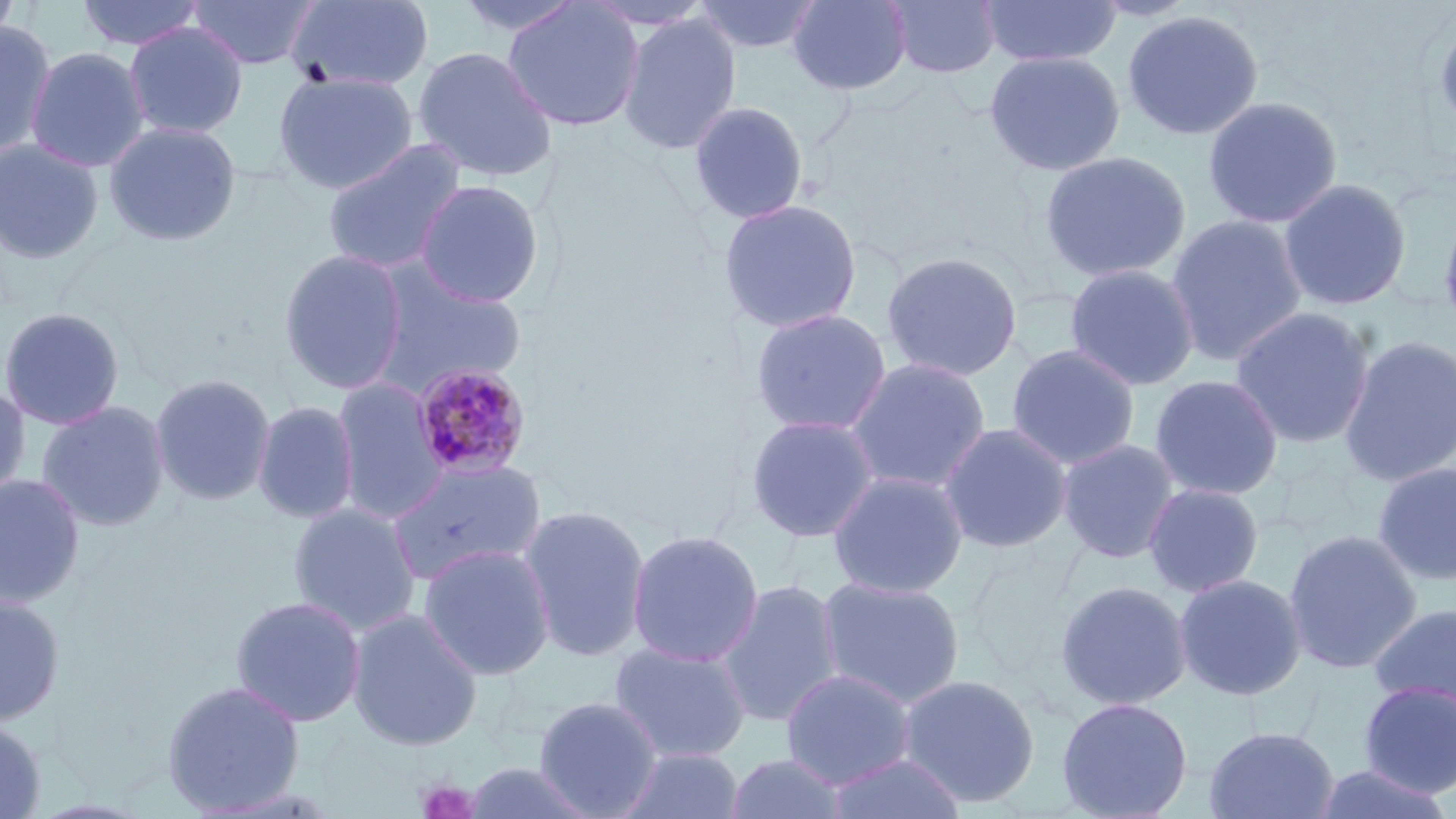
slide-level diagnosis = Plasmodium malariae
modality = light microscopy
magnification = 1000x
stain = May-Grünwald-Giemsa
uninfected red blood cell locations = approximate bounding boxes as (x1,y1)-(x2,y2) corner pairs in pixels: (0,0)-(21,52), (74,0)-(207,52), (185,0)-(321,70), (285,0)-(436,93), (455,0)-(585,39), (502,0)-(645,132), (692,0)-(824,55), (787,0)-(912,95), (886,0)-(1002,79), (979,0)-(1122,67), (1122,10)-(1264,140), (1434,10)-(1456,141), (618,12)-(742,155), (0,21)-(57,159), (124,22)-(248,139), (411,45)-(559,183), (25,46)-(150,173), (984,50)-(1125,176), (272,71)-(418,195), (1203,96)-(1343,229), (687,100)-(810,225), (103,121)-(242,246), (0,139)-(105,264), (321,139)-(468,275), (1038,150)-(1192,284), (1277,178)-(1412,311), (413,179)-(547,308), (718,198)-(863,334), (1437,198)-(1456,342), (1166,214)-(1308,367), (277,248)-(410,395), (880,250)-(1023,382), (366,261)-(527,394), (1064,263)-(1200,391), (1229,305)-(1376,449), (0,307)-(125,431), (749,307)-(893,436), (1338,334)-(1456,487), (1006,344)-(1141,470), (844,356)-(992,493), (149,372)-(277,506), (1149,374)-(1284,501), (331,377)-(447,523), (0,384)-(31,505), (36,400)-(171,532), (251,400)-(360,525), (744,414)-(881,543), (938,422)-(1073,554), (1057,438)-(1181,564), (386,458)-(547,585), (1371,460)-(1456,586), (827,469)-(969,599), (0,474)-(85,609), (1142,482)-(1264,598), (287,502)-(422,636), (516,504)-(651,661), (625,529)-(764,667), (1283,529)-(1422,674), (417,542)-(556,681), (1172,572)-(1308,701), (816,575)-(966,709), (715,578)-(845,728), (1054,579)-(1192,711), (0,592)-(65,727), (230,596)-(366,728), (1366,601)-(1456,717), (346,608)-(484,751), (609,641)-(752,761), (780,668)-(916,789), (897,672)-(1041,808), (161,679)-(306,815), (1357,680)-(1456,797), (532,696)-(664,818), (1055,696)-(1193,819), (0,716)-(46,818), (1203,725)-(1339,818), (617,747)-(745,819), (823,751)-(965,818), (724,752)-(849,818), (459,761)-(599,818), (1309,763)-(1454,819)
platelet locations = approximate bounding boxes as (x1,y1)-(x2,y2) corner pairs in pixels: (417,778)-(480,819)
image size = 1456×819 pixels
field of view = one of a larger specimen
preparation = thin blood film
Plasmodium malariae-infected red blood cell locations = approximate bounding boxes as (x1,y1)-(x2,y2) corner pairs in pixels: (410,362)-(532,481)